Comment on the morphology of the erythrocytes.
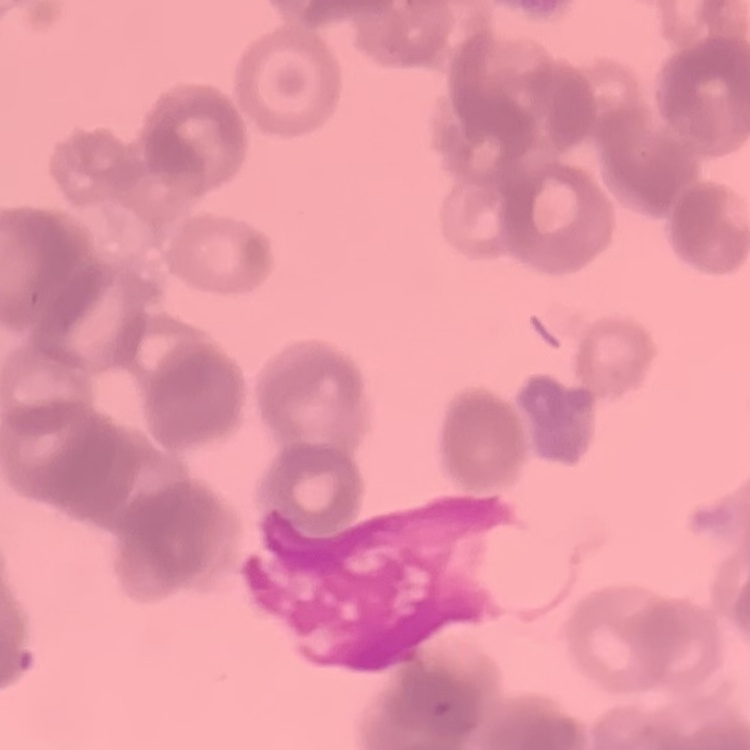

Rouleaux formation.

Thin peripheral smear. Field's or Giemsa stain. Square crop of a larger photomicrograph.